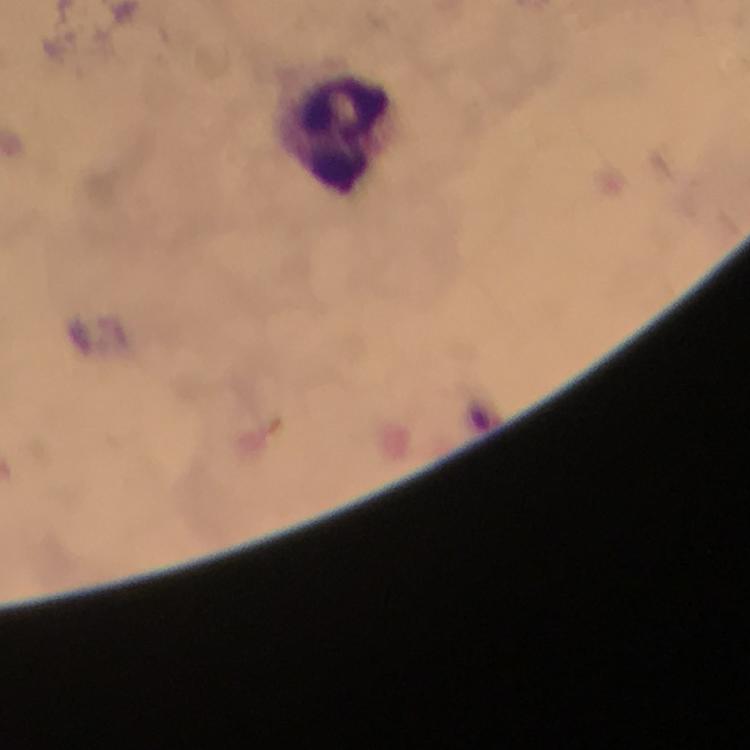

{
  "leukocyte_locations": "approximate centers as (x, y) in pixels: (344, 131)",
  "capture": "smartphone camera through the microscope",
  "preparation": "thick smear",
  "cropped_from": "one field of view",
  "immersion_oil": "applied",
  "stain": "Giemsa",
  "context": "from a malaria diagnostic workup",
  "magnification": "100x",
  "image_size": "750×750 pixels",
  "plasmodium_parasites": "none detected"
}